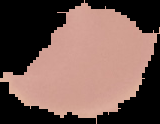
Summary:
  - Image size: 160×124 pixels
  - Preparation: thin blood film
  - Result: no malaria parasites detected
  - Image type: segmented cell region on a black background